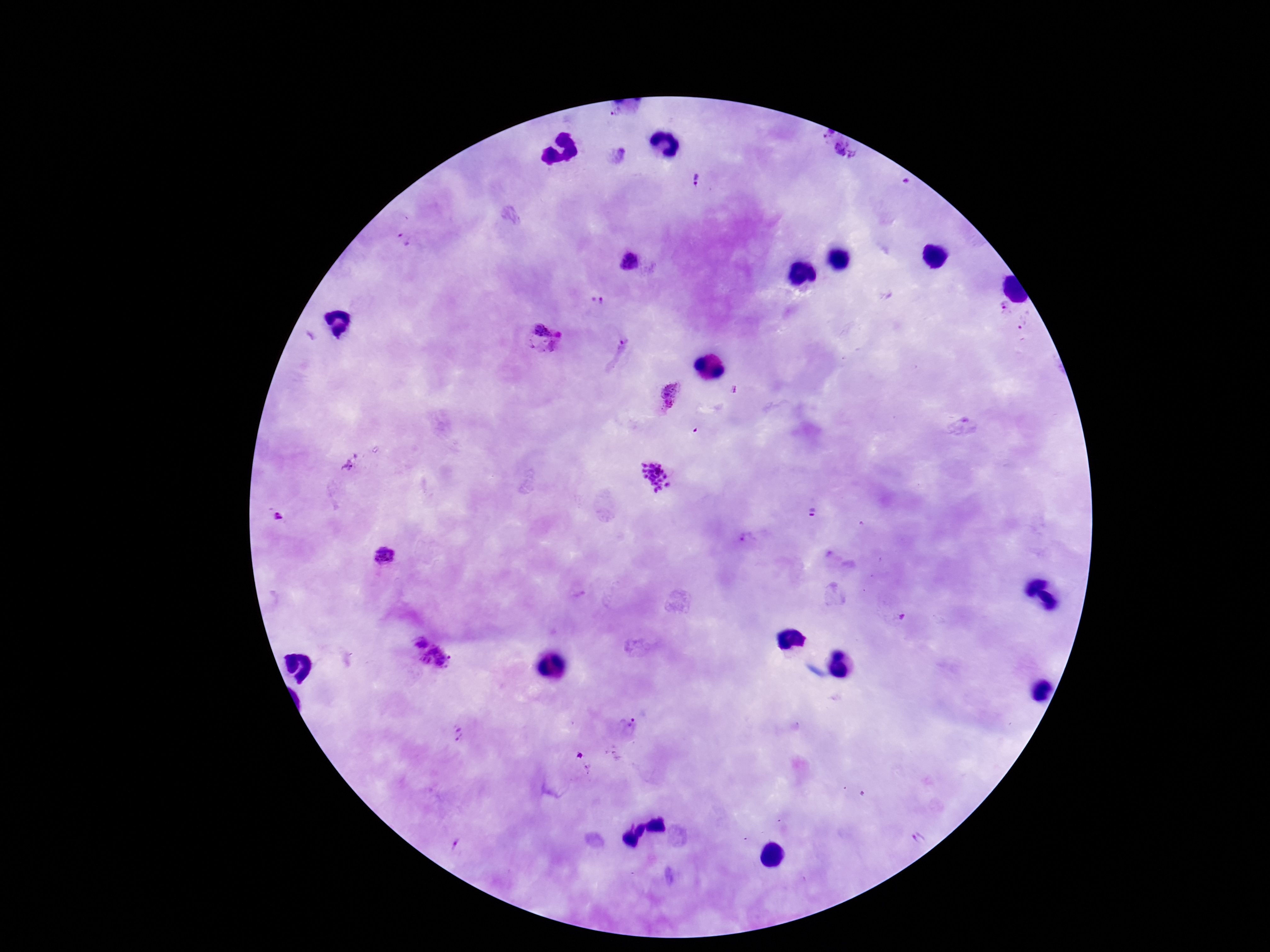

patient malaria status = positive
capture = smartphone camera through the microscope eyepiece
preparation = thick blood film
image size = 1270×952 pixels
field of view = one from this slide
magnification = 100x
stain = Giemsa
Plasmodium parasite locations = approximate centers as [x, y] in pixels: [843, 151], [697, 179], [404, 239], [630, 263], [602, 301], [1003, 307], [542, 334], [672, 396], [655, 475], [811, 513], [278, 518], [747, 539], [384, 557], [419, 642], [438, 660], [632, 723], [459, 734]